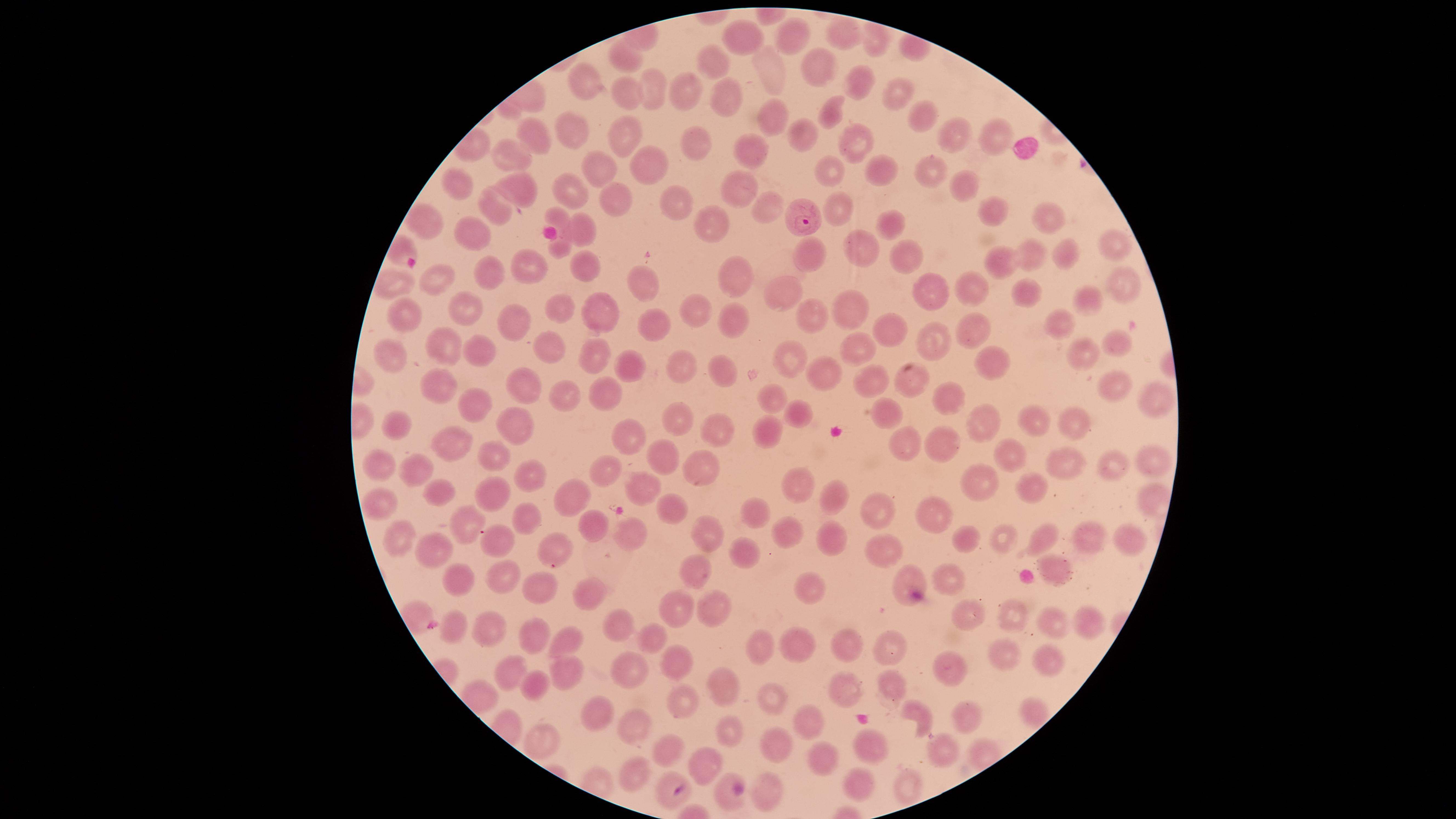

capture = smartphone photograph through the microscope eyepiece
species = Plasmodium falciparum
presence = malaria parasites seen
visible region = circular
field of view = single
preparation = thin blood film
uninfected red blood cells = approximate marker points, in pixels from the top-left corner: (x=841, y=36), (x=793, y=37), (x=743, y=40), (x=625, y=56), (x=711, y=63), (x=813, y=65), (x=766, y=71), (x=859, y=83), (x=586, y=85), (x=650, y=90), (x=899, y=92), (x=686, y=93), (x=626, y=96), (x=725, y=100), (x=829, y=112), (x=921, y=115), (x=768, y=117), (x=573, y=133), (x=625, y=133), (x=797, y=133), (x=534, y=134), (x=993, y=137), (x=956, y=138), (x=696, y=139), (x=856, y=140), (x=513, y=153), (x=752, y=155), (x=647, y=163), (x=597, y=168), (x=835, y=168), (x=880, y=168), (x=925, y=170), (x=518, y=181), (x=462, y=185), (x=963, y=185), (x=741, y=188), (x=570, y=193), (x=676, y=202), (x=615, y=205), (x=768, y=205), (x=840, y=206), (x=989, y=210), (x=497, y=211), (x=1055, y=219), (x=558, y=220), (x=703, y=222), (x=425, y=225), (x=893, y=225), (x=586, y=230), (x=473, y=232), (x=1116, y=243), (x=861, y=250), (x=805, y=253), (x=1067, y=255), (x=1035, y=256), (x=904, y=258), (x=529, y=264), (x=1006, y=266), (x=587, y=270), (x=488, y=277), (x=740, y=278), (x=1119, y=278), (x=438, y=280), (x=390, y=283), (x=641, y=286), (x=787, y=289), (x=966, y=289), (x=936, y=292), (x=1023, y=295), (x=1083, y=299), (x=468, y=306), (x=696, y=308), (x=851, y=309), (x=564, y=310), (x=604, y=312), (x=813, y=312), (x=398, y=313), (x=1063, y=316), (x=738, y=323), (x=513, y=327), (x=661, y=329), (x=978, y=332), (x=890, y=334), (x=935, y=338), (x=1121, y=343), (x=446, y=344), (x=479, y=347), (x=554, y=348), (x=595, y=349), (x=857, y=349), (x=1081, y=354), (x=391, y=355), (x=787, y=356), (x=992, y=361), (x=684, y=367), (x=633, y=368), (x=726, y=372), (x=823, y=380), (x=875, y=381), (x=913, y=381), (x=1115, y=382), (x=443, y=384), (x=530, y=384), (x=604, y=393), (x=571, y=398), (x=1148, y=399), (x=776, y=400), (x=952, y=402), (x=471, y=410), (x=883, y=411), (x=807, y=417), (x=1035, y=421), (x=985, y=422), (x=673, y=423), (x=1073, y=426), (x=508, y=427), (x=723, y=427), (x=402, y=429), (x=772, y=433), (x=627, y=441), (x=910, y=444), (x=455, y=446), (x=949, y=446), (x=490, y=456), (x=1019, y=459), (x=1156, y=463), (x=385, y=465), (x=671, y=465), (x=416, y=467), (x=1075, y=467), (x=1116, y=467), (x=609, y=470), (x=705, y=470), (x=531, y=476), (x=984, y=478), (x=1031, y=484), (x=642, y=487), (x=802, y=489), (x=497, y=491), (x=440, y=492), (x=832, y=494), (x=577, y=502), (x=380, y=503), (x=669, y=510), (x=881, y=511), (x=760, y=515), (x=930, y=515), (x=461, y=521), (x=531, y=521), (x=631, y=527), (x=594, y=531), (x=790, y=533), (x=715, y=535), (x=1092, y=536), (x=828, y=537), (x=965, y=537), (x=1000, y=537), (x=1040, y=537), (x=402, y=539), (x=498, y=541), (x=1132, y=542), (x=884, y=546), (x=748, y=547), (x=443, y=548), (x=549, y=548), (x=693, y=569), (x=1059, y=569), (x=953, y=577), (x=498, y=580), (x=461, y=583), (x=906, y=583), (x=539, y=586), (x=812, y=592), (x=594, y=593), (x=711, y=602), (x=679, y=611), (x=1013, y=616), (x=966, y=617), (x=1083, y=620), (x=617, y=621), (x=1057, y=623), (x=487, y=627), (x=457, y=631), (x=534, y=633), (x=573, y=640), (x=656, y=640), (x=845, y=644), (x=804, y=647), (x=763, y=649), (x=894, y=650), (x=1002, y=655), (x=673, y=660), (x=1051, y=661), (x=949, y=668), (x=572, y=669), (x=630, y=669), (x=519, y=673), (x=888, y=682), (x=720, y=683), (x=540, y=685), (x=853, y=693), (x=774, y=697), (x=688, y=704), (x=1034, y=708), (x=600, y=709), (x=918, y=716), (x=970, y=717), (x=800, y=721), (x=633, y=728), (x=727, y=735), (x=552, y=740), (x=776, y=740), (x=872, y=743), (x=947, y=750), (x=666, y=751), (x=832, y=760), (x=707, y=763), (x=640, y=770), (x=856, y=780), (x=913, y=786), (x=724, y=794), (x=765, y=796)
stain = Giemsa
image size = 1456×819 pixels
parasitized red blood cells = approximate marker points, in pixels from the top-left corner: (x=803, y=209), (x=669, y=787)